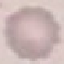
Result: negative for malaria parasites. Photographed with a smartphone camera at the microscope eyepiece. Thin blood smear. Giemsa stain. Cell patch, automatically extracted from a larger field of view and resized to 64 × 64 pixels.